Name the parasite shown.
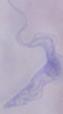

This is a trypanosome.

Micrograph. 1000x magnification.